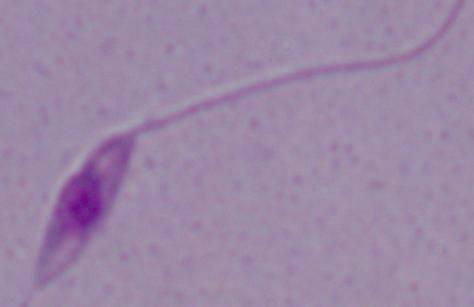

modality: micrograph
identification: Leishmania
magnification: 1000x